Locate every leukocyte (white blood cell).
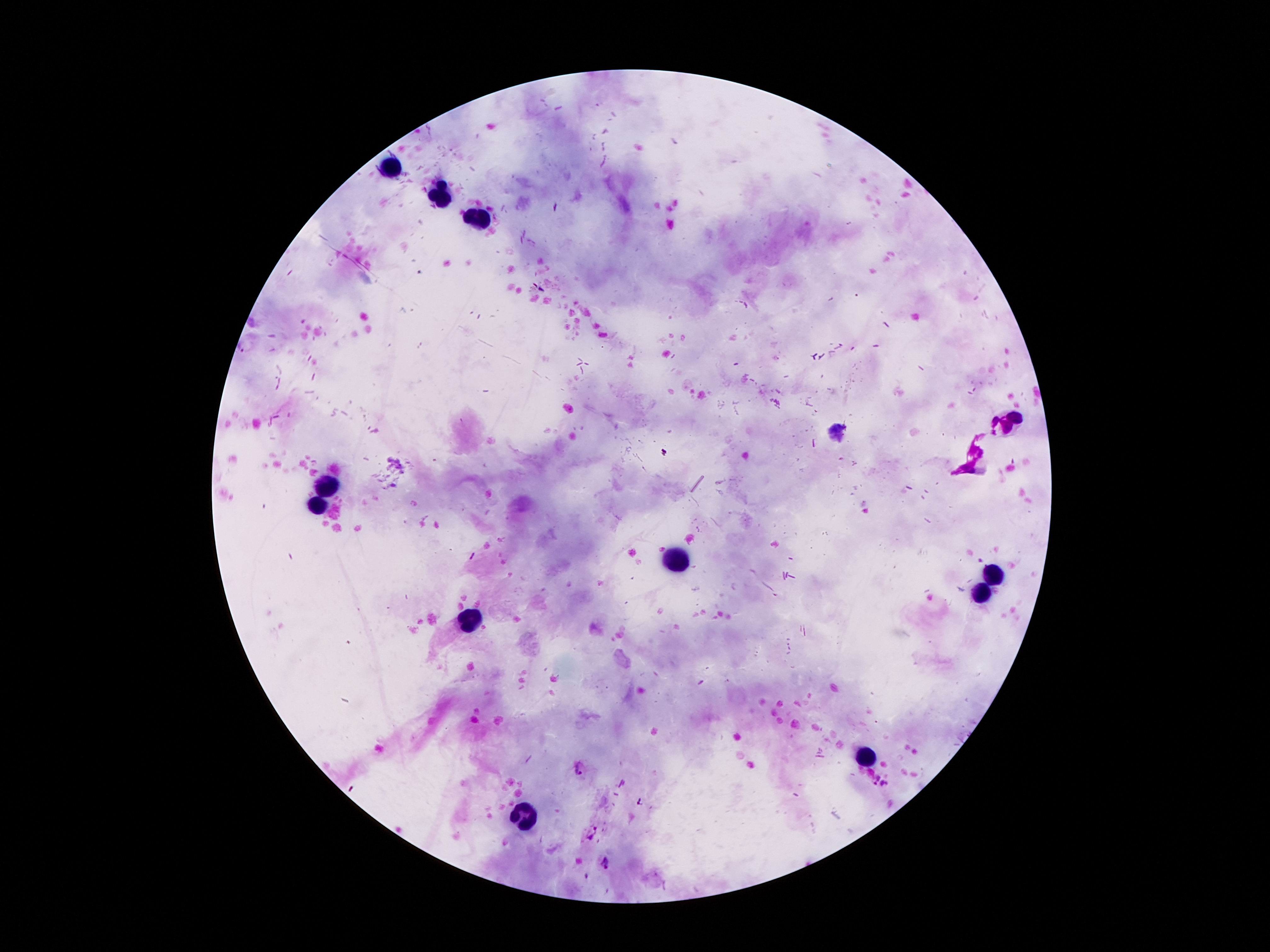
Approximate centers as (x, y) in pixels.
Leukocytes: (391, 167), (438, 194), (477, 221), (1009, 420), (324, 483), (318, 504), (678, 560), (997, 574), (980, 595), (467, 618), (868, 756), (522, 815).

field_of_view: single
preparation: thick blood smear
magnification: 100x
image_size: 1270×952 pixels
stain: Giemsa
malaria_parasite_locations: 'approximate centers as (x, y) in pixels: (580, 768), (872, 778), (885, 785), (591, 831), (604, 863)'
capture: smartphone through the microscope eyepiece
patient_malaria_status: positive for Plasmodium falciparum